Name the parasite shown.
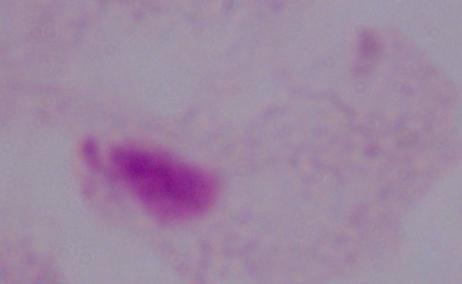
This is a trichomonad.

modality = photomicrograph
magnification = 1000x